Report the malaria status of this cell.
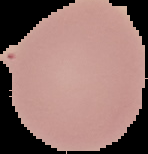

It is uninfected.

preparation = thin blood smear
image size = 148×154 pixels
image type = segmented cell region on a black background